Report the malaria status of this cell.
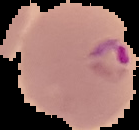

Parasitized.

image size = 139×130 pixels
image type = segmented cell region with the area outside set to black
preparation = thin blood film